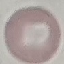 Result: no malaria parasites seen. Cell patch, automatically extracted from a larger field of view and resized to 64 × 64 pixels. Giemsa-stained preparation. Acquired by smartphone through the microscope eyepiece. Thin blood smear.